State which parasite is depicted.
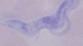
A trypanosome.

modality = photomicrograph
magnification = 1000x